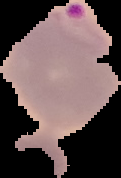
Result: malaria parasites identified. Image is 121×178 pixels. Cell region segmented out of the field of view; the surrounding area is masked to black. From a thin blood smear.